Point out each malaria parasite and each leukocyte.
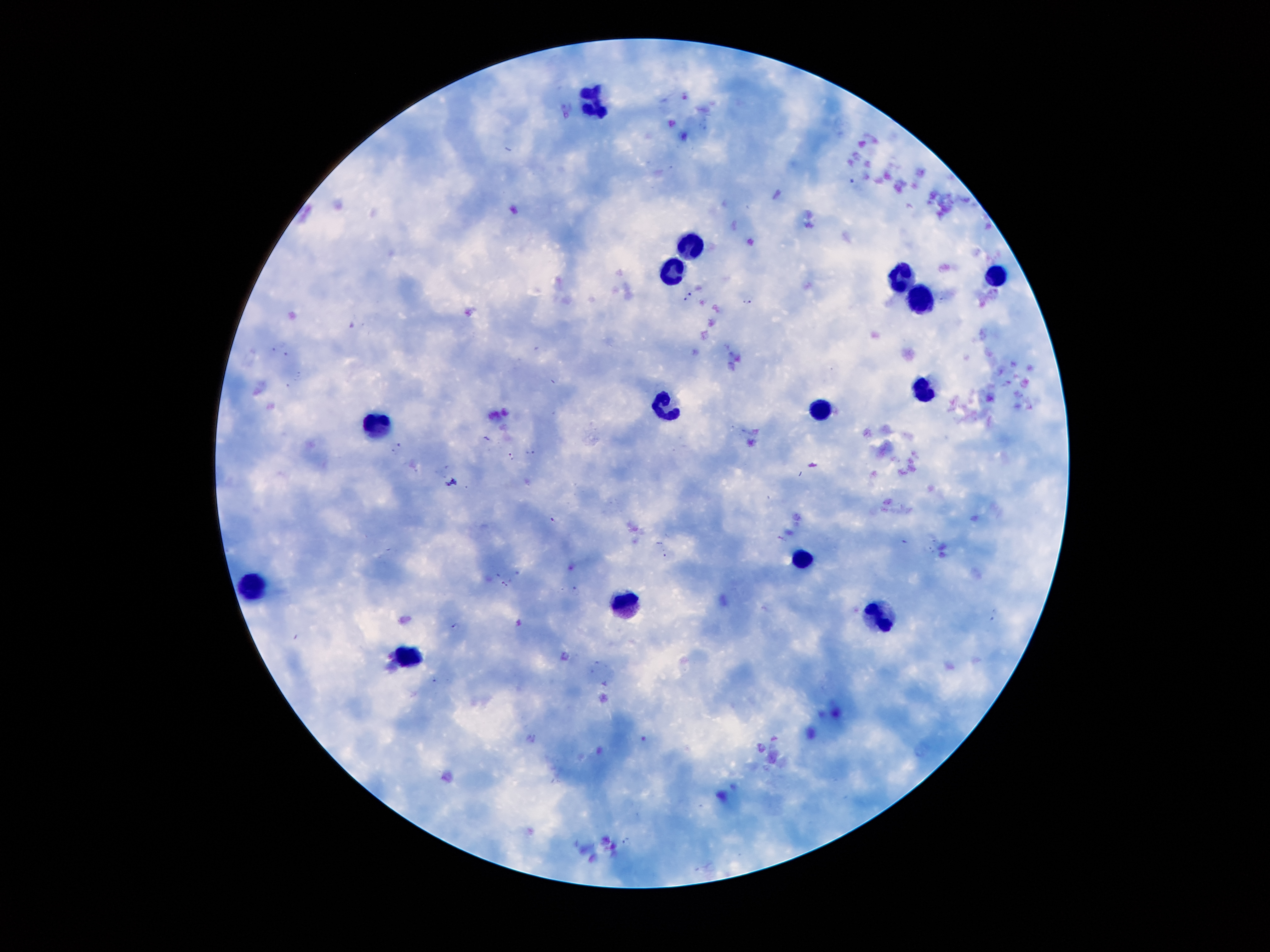

Approximate centers as (x, y) in pixels.
Malaria parasites: (688, 296), (747, 299), (531, 451), (511, 456), (451, 481), (552, 519), (665, 554), (505, 585), (575, 591), (454, 625), (627, 841).
Leukocytes: (593, 99), (698, 242), (670, 273), (994, 274), (902, 276), (923, 306), (923, 393), (666, 407), (820, 408), (374, 427), (800, 557), (249, 586), (630, 608), (883, 617), (407, 653).

Giemsa-stained preparation. Single field of view. 100x magnification. Image is 1270×952 pixels. Patient malaria status: positive for Plasmodium falciparum. Thick blood smear. Photographed through the microscope eyepiece with a smartphone camera.